Locate platelets.
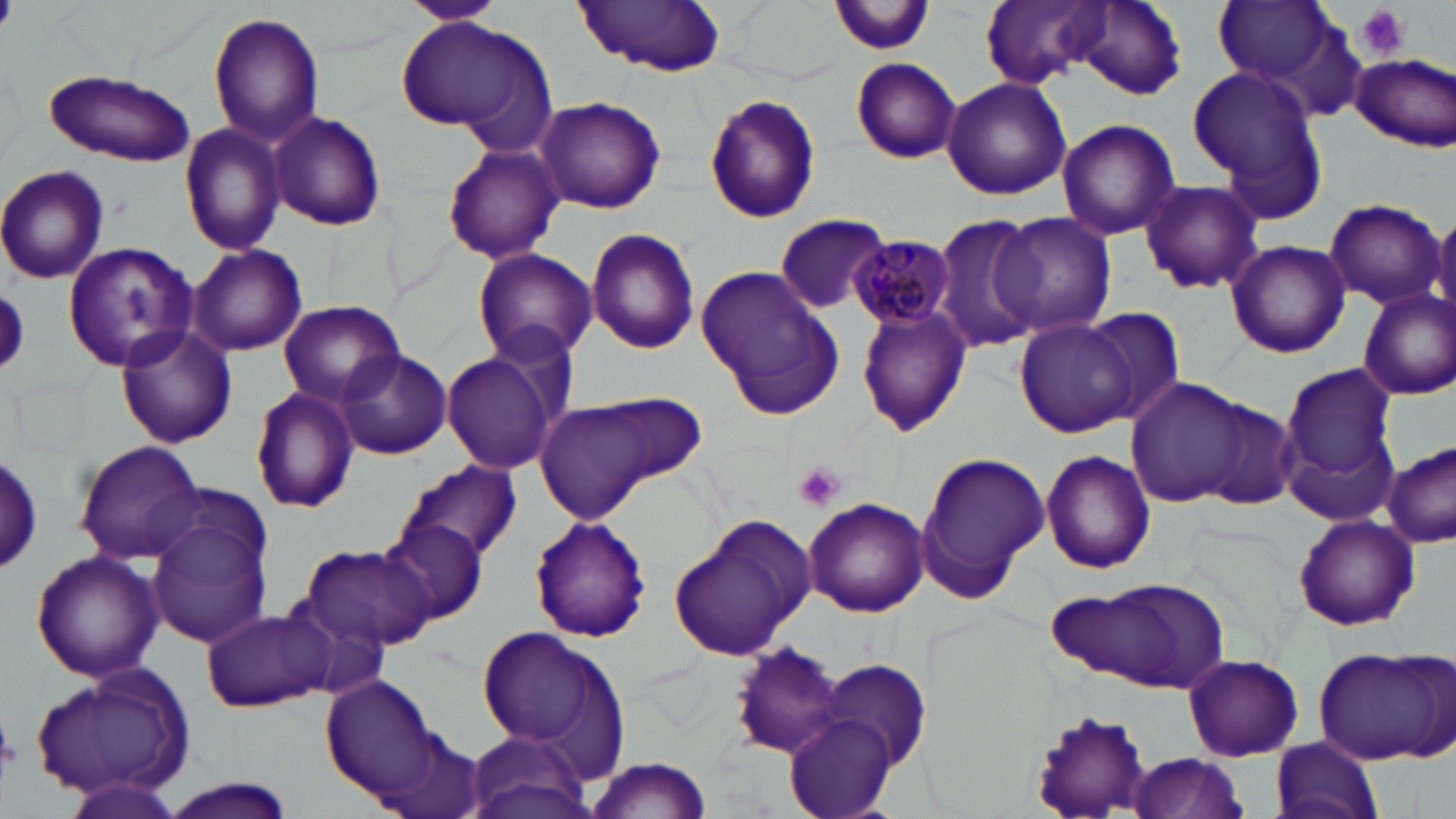
Approximate bounding boxes as [x1, y1, x2, y2] in pixels.
Platelets: [0, 0, 14, 31], [1356, 5, 1411, 59], [794, 462, 847, 512].

slide-level diagnosis = Plasmodium malariae
preparation = thin blood smear
stain = May-Grünwald-Giemsa
modality = optical microscopy
image size = 1456×819 pixels
Plasmodium malariae-infected red blood cell locations = approximate bounding boxes as [x1, y1, x2, y2] in pixels: [849, 234, 957, 328]
uninfected red blood cell locations = approximate bounding boxes as [x1, y1, x2, y2] in pixels: [402, 0, 504, 24], [726, 0, 849, 88], [1061, 0, 1187, 101], [575, 1, 729, 77], [833, 1, 938, 55], [980, 1, 1106, 88], [1213, 1, 1342, 89], [207, 12, 326, 147], [394, 16, 554, 144], [1350, 54, 1455, 149], [849, 57, 960, 163], [1191, 65, 1328, 212], [40, 68, 196, 168], [941, 76, 1071, 201], [702, 93, 823, 223], [536, 97, 666, 214], [268, 110, 386, 231], [1056, 118, 1180, 241], [179, 121, 289, 257], [442, 142, 564, 265], [0, 166, 109, 284], [1136, 180, 1265, 295], [1320, 198, 1446, 308], [992, 211, 1118, 336], [773, 212, 892, 314], [932, 212, 1045, 355], [1429, 212, 1456, 330], [585, 227, 701, 356], [62, 240, 198, 372], [1224, 241, 1351, 358], [187, 244, 307, 357], [473, 248, 598, 366], [695, 267, 846, 419], [1356, 287, 1456, 402], [278, 299, 404, 406], [856, 304, 972, 435], [1082, 306, 1187, 426], [1014, 318, 1137, 439], [114, 322, 238, 449], [334, 349, 451, 459], [443, 352, 555, 474], [1280, 361, 1398, 500], [1124, 378, 1250, 509], [249, 386, 361, 515], [532, 396, 685, 524], [1193, 396, 1302, 512], [74, 439, 205, 563], [1382, 443, 1455, 546], [915, 450, 1051, 604], [1040, 450, 1157, 575], [2, 451, 42, 577], [402, 461, 521, 559], [803, 496, 929, 617], [144, 505, 273, 649], [380, 515, 488, 626], [529, 515, 652, 644], [1293, 515, 1420, 630], [668, 516, 819, 662], [299, 542, 435, 653], [30, 549, 163, 683], [1066, 575, 1230, 694], [201, 608, 329, 712], [477, 623, 632, 773], [727, 642, 845, 759], [1313, 645, 1452, 765], [1182, 655, 1304, 762], [817, 659, 932, 772], [34, 662, 198, 807], [324, 675, 441, 801], [780, 713, 900, 819], [1031, 714, 1154, 816], [466, 729, 594, 819], [1268, 735, 1382, 819], [1120, 753, 1254, 819], [584, 757, 713, 818], [60, 777, 187, 819], [159, 777, 298, 819]
field of view = one of a larger specimen
magnification = 1000x